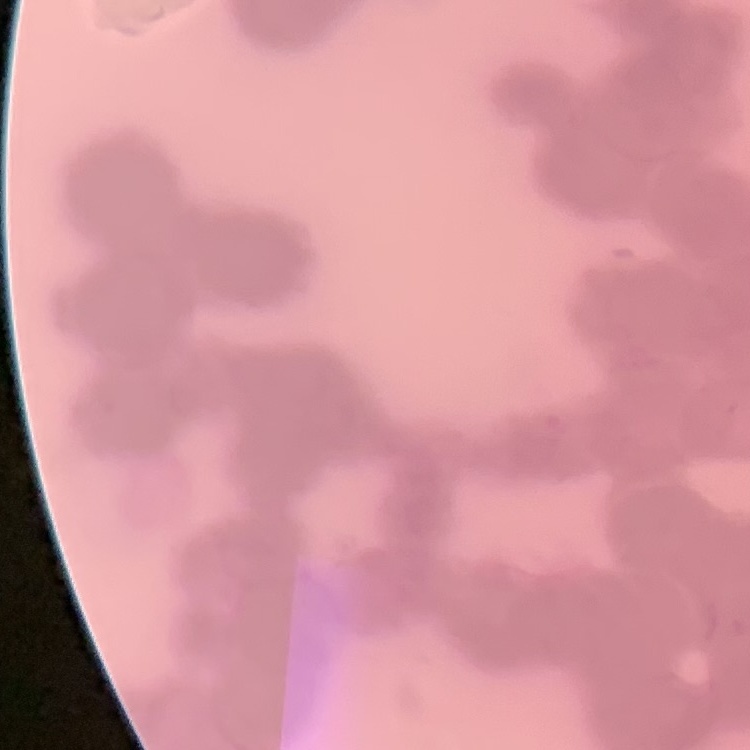
red blood cell morphology = rouleaux formation
stain = Field's or Giemsa
preparation = thin peripheral smear
image type = one tile cut from a larger photomicrograph